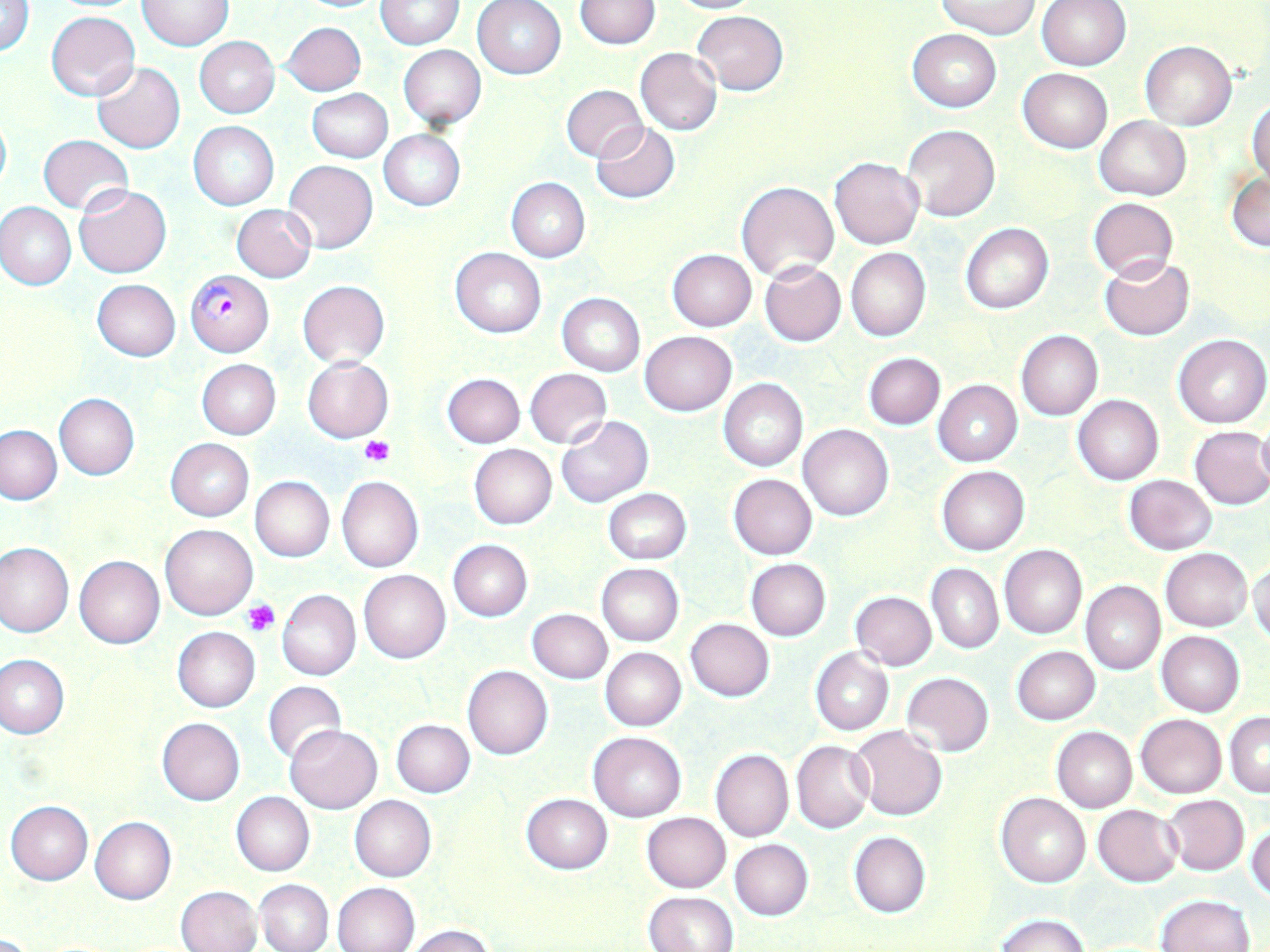 Approximate bounding boxes as [x1, y1, x2, y2] in pixels. Plasmodium falciparum-infected red blood cell locations: [186, 270, 273, 356]. Uninfected red blood cell locations: [374, 0, 462, 48], [575, 0, 660, 49], [664, 0, 767, 14], [937, 0, 1041, 38], [138, 1, 232, 50], [291, 1, 389, 13], [473, 1, 566, 80], [1038, 1, 1130, 71], [1, 2, 34, 58], [46, 10, 140, 101], [694, 10, 788, 94], [281, 21, 366, 96], [908, 28, 1001, 112], [194, 36, 280, 118], [1140, 41, 1236, 131], [397, 45, 486, 129], [634, 48, 722, 135], [92, 63, 186, 153], [1018, 68, 1112, 153], [560, 84, 649, 163], [305, 88, 393, 162], [1247, 96, 1270, 186], [0, 110, 11, 196], [1095, 116, 1191, 199], [189, 122, 279, 210], [591, 123, 679, 203], [902, 124, 1000, 221], [378, 129, 465, 211], [38, 134, 132, 215], [830, 157, 923, 248], [283, 159, 378, 254], [1227, 172, 1269, 253], [506, 178, 589, 262], [737, 181, 838, 279], [74, 184, 172, 278], [1087, 198, 1178, 281], [0, 203, 75, 290], [231, 204, 316, 283], [960, 223, 1053, 314], [846, 247, 931, 342], [450, 248, 545, 337], [667, 249, 756, 330], [1099, 255, 1194, 341], [759, 261, 846, 346], [92, 279, 180, 360], [297, 280, 389, 367], [558, 294, 645, 375], [1016, 330, 1102, 421], [640, 331, 736, 416], [1173, 334, 1270, 428], [863, 353, 945, 430], [303, 357, 392, 442], [197, 359, 281, 440], [524, 368, 613, 449], [442, 373, 525, 447], [719, 378, 808, 471], [933, 379, 1022, 467], [54, 394, 140, 479], [1072, 394, 1163, 485], [556, 415, 653, 507], [1255, 421, 1270, 495], [799, 424, 894, 521], [0, 425, 64, 504], [1190, 427, 1270, 510], [166, 438, 254, 520], [468, 443, 557, 529], [937, 465, 1029, 556], [727, 473, 818, 559], [1125, 475, 1217, 554], [250, 476, 335, 562], [337, 476, 423, 572], [603, 489, 691, 564], [161, 524, 258, 619], [447, 540, 532, 622], [0, 542, 73, 638], [1000, 545, 1087, 639], [1161, 548, 1252, 631], [74, 555, 165, 649], [745, 558, 831, 640], [1249, 558, 1269, 645], [596, 563, 683, 647], [926, 563, 1003, 654], [358, 569, 451, 664], [853, 579, 999, 659], [1081, 581, 1164, 675], [277, 590, 361, 680], [850, 591, 937, 670], [526, 609, 612, 684], [686, 619, 775, 702], [172, 627, 260, 711], [1156, 631, 1245, 716], [600, 646, 686, 730], [1011, 646, 1100, 725], [810, 647, 893, 735], [1, 655, 69, 738], [462, 664, 553, 759], [902, 672, 994, 757], [263, 680, 347, 767], [1226, 711, 1270, 797], [1135, 714, 1227, 798], [157, 718, 245, 804], [391, 719, 475, 797], [285, 725, 382, 813], [850, 727, 948, 821], [1052, 727, 1137, 812], [589, 731, 686, 820], [792, 741, 872, 833], [710, 749, 793, 843], [232, 792, 314, 875], [997, 792, 1090, 888], [521, 793, 613, 874], [350, 795, 436, 881], [1163, 795, 1249, 876], [5, 801, 93, 884], [1093, 804, 1183, 886], [642, 812, 731, 892], [90, 816, 177, 904], [1247, 819, 1269, 902], [848, 831, 930, 918], [730, 839, 813, 920], [255, 879, 333, 952], [332, 882, 420, 951], [175, 885, 261, 952], [644, 891, 739, 952], [1155, 894, 1253, 952], [998, 914, 1089, 952], [401, 925, 496, 952]. Platelet locations: [359, 437, 395, 467], [245, 600, 279, 637]. Slide-level diagnosis: Plasmodium falciparum. Light microscopy. May-Grünwald-Giemsa stain. 1000x magnification. One field of a larger specimen. Thin blood film. Image is 1270×952 pixels.